Assess the morphology of the erythrocytes.
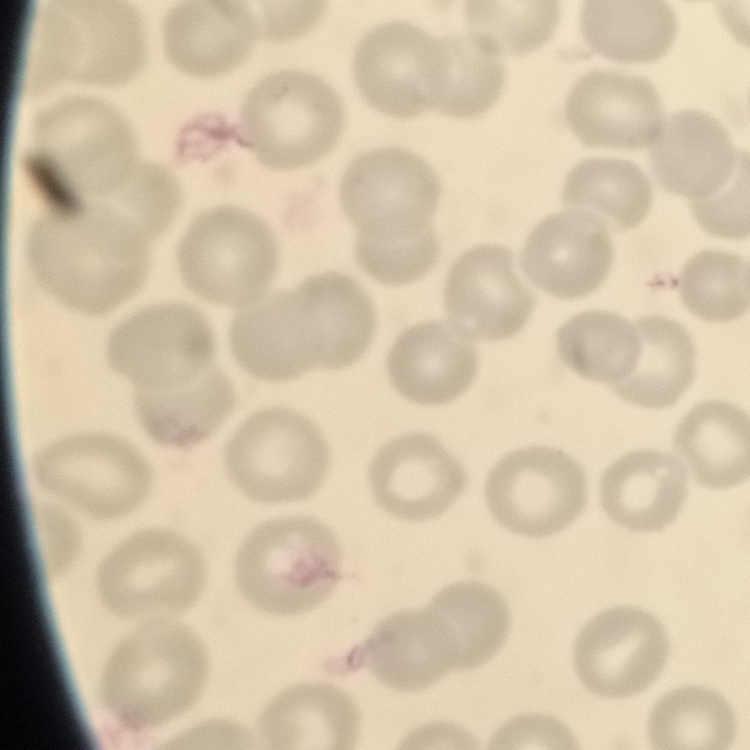
No rouleaux formation.

{
  "stain": "Field's or Giemsa",
  "preparation": "thin blood smear",
  "image_type": "square crop of a larger photomicrograph"
}